Rate the background quality.
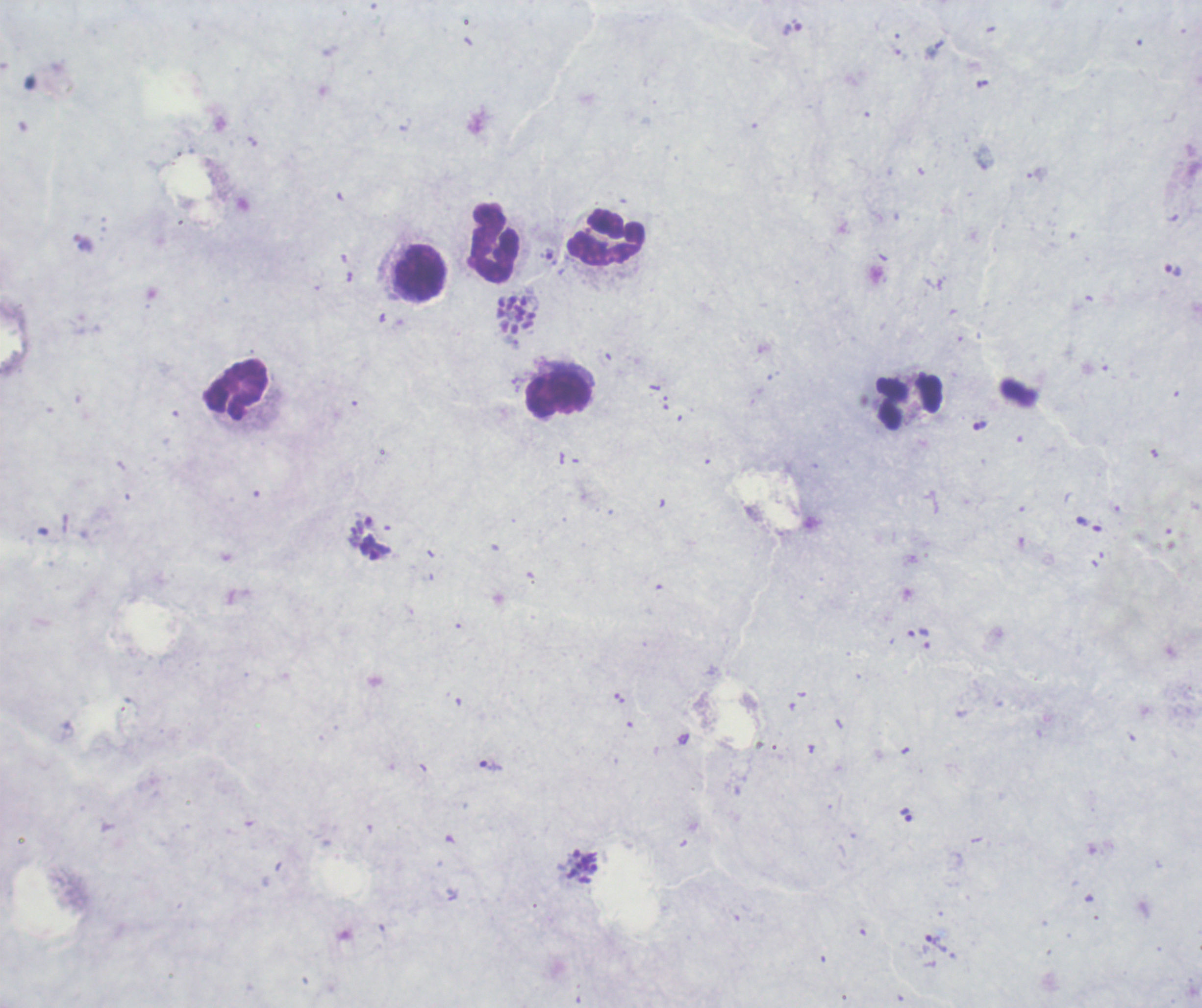

Poor.

Approximate centers as [x, y] in pixels.
Summary:
  - Leukocyte locations: [607, 237], [493, 243], [422, 274], [236, 390], [559, 395], [910, 405]
  - Trophozoite locations: [546, 254], [1174, 271], [376, 547], [918, 632], [490, 766], [906, 815], [937, 942]
  - Schizont locations: [518, 316], [583, 867]
  - Life-cycle stages observed: trophozoite, schizont
  - Stain: Romanowsky
  - Magnification: 100x
  - Preparation: thick smear of blood
  - Field of view: single
  - Context: previously used in an actual diagnosis
  - Result: positive for Plasmodium parasites
  - Image size: 1202×1008 pixels